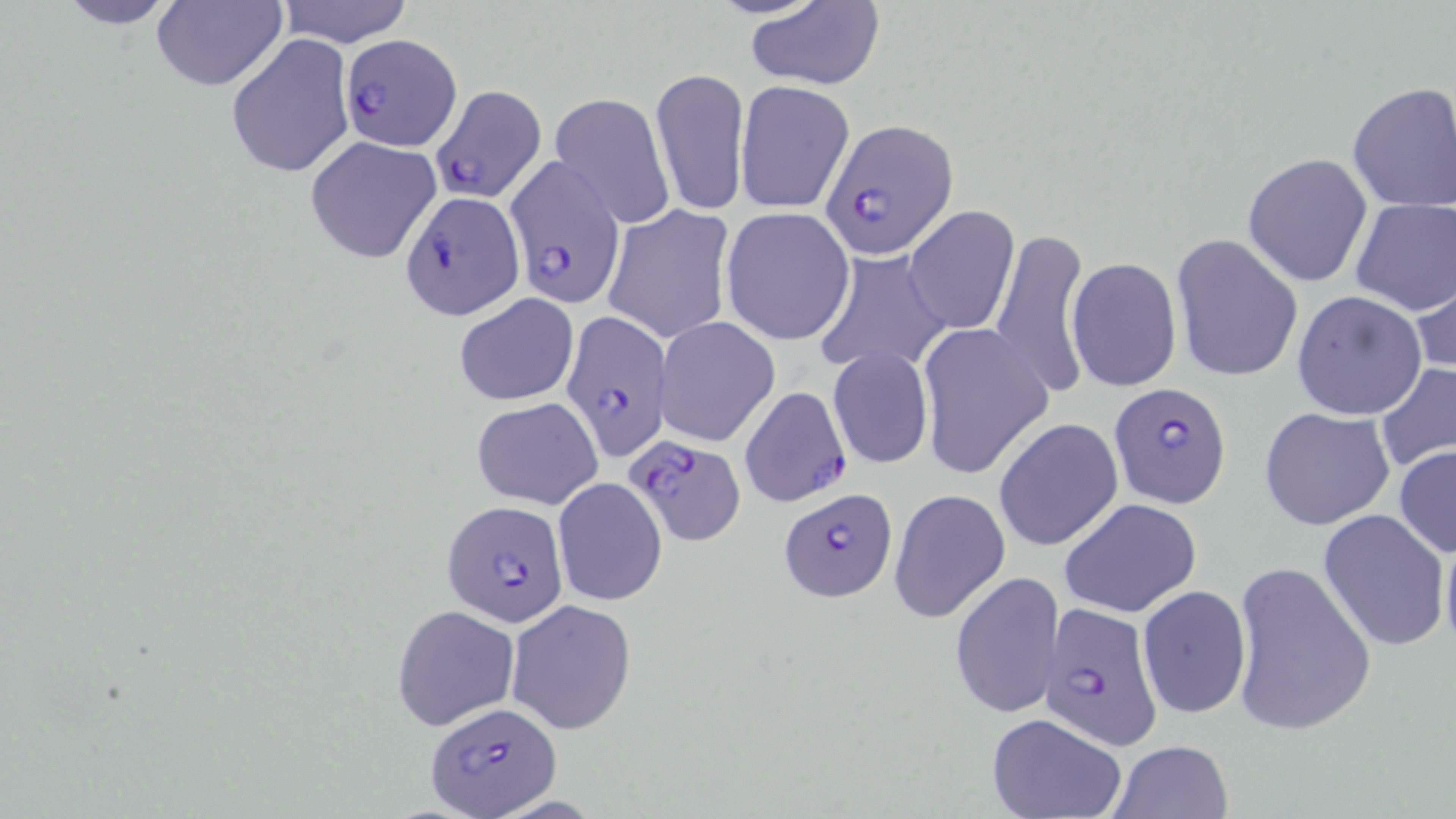
slide_level_diagnosis: Plasmodium falciparum
modality: light microscopy
plasmodium_falciparum_infected_red_blood_cell_locations: 'approximate bounding boxes as (x1, y1, x2, y2) in pixels: (340, 33, 462, 150), (430, 83, 547, 205), (821, 117, 960, 259), (503, 157, 624, 306), (400, 189, 522, 320), (561, 310, 670, 460), (1108, 383, 1232, 508), (739, 385, 851, 508), (624, 434, 744, 545), (780, 487, 900, 604), (443, 501, 570, 625), (1041, 603, 1165, 748), (426, 700, 559, 818)'
uninfected_red_blood_cell_locations: 'approximate bounding boxes as (x1, y1, x2, y2) in pixels: (47, 0, 190, 29), (275, 0, 415, 47), (149, 1, 286, 92), (743, 2, 886, 89), (227, 35, 354, 180), (651, 66, 750, 217), (735, 80, 855, 215), (1347, 82, 1456, 213), (549, 92, 675, 229), (304, 136, 442, 265), (1242, 152, 1373, 288), (1349, 197, 1456, 316), (601, 204, 736, 345), (904, 205, 1019, 335), (721, 207, 855, 344), (990, 228, 1091, 399), (1170, 234, 1302, 382), (813, 250, 951, 377), (1066, 256, 1182, 392), (1411, 266, 1456, 382), (1291, 291, 1427, 420), (453, 292, 579, 407), (655, 316, 780, 446), (917, 322, 1052, 482), (828, 347, 933, 470), (1376, 364, 1456, 474), (471, 396, 604, 509), (1260, 407, 1395, 532), (994, 418, 1124, 553), (1393, 445, 1456, 559), (552, 477, 667, 606), (889, 488, 1010, 624), (1059, 497, 1201, 618), (1319, 509, 1450, 652), (1439, 521, 1456, 662), (1229, 561, 1377, 737), (949, 573, 1066, 718), (1137, 584, 1253, 719), (505, 600, 637, 736), (392, 604, 520, 730), (985, 713, 1128, 819), (1106, 739, 1235, 819)'
field_of_view: one of a larger specimen
image_size: 1456×819 pixels
stain: May-Grünwald-Giemsa
magnification: 1000x
preparation: thin blood film